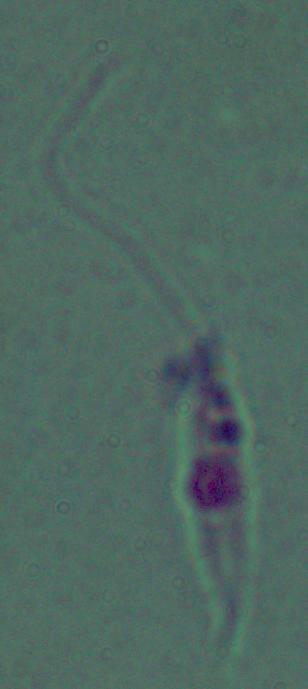
identification: Leishmania
magnification: 1000x
modality: photomicrograph